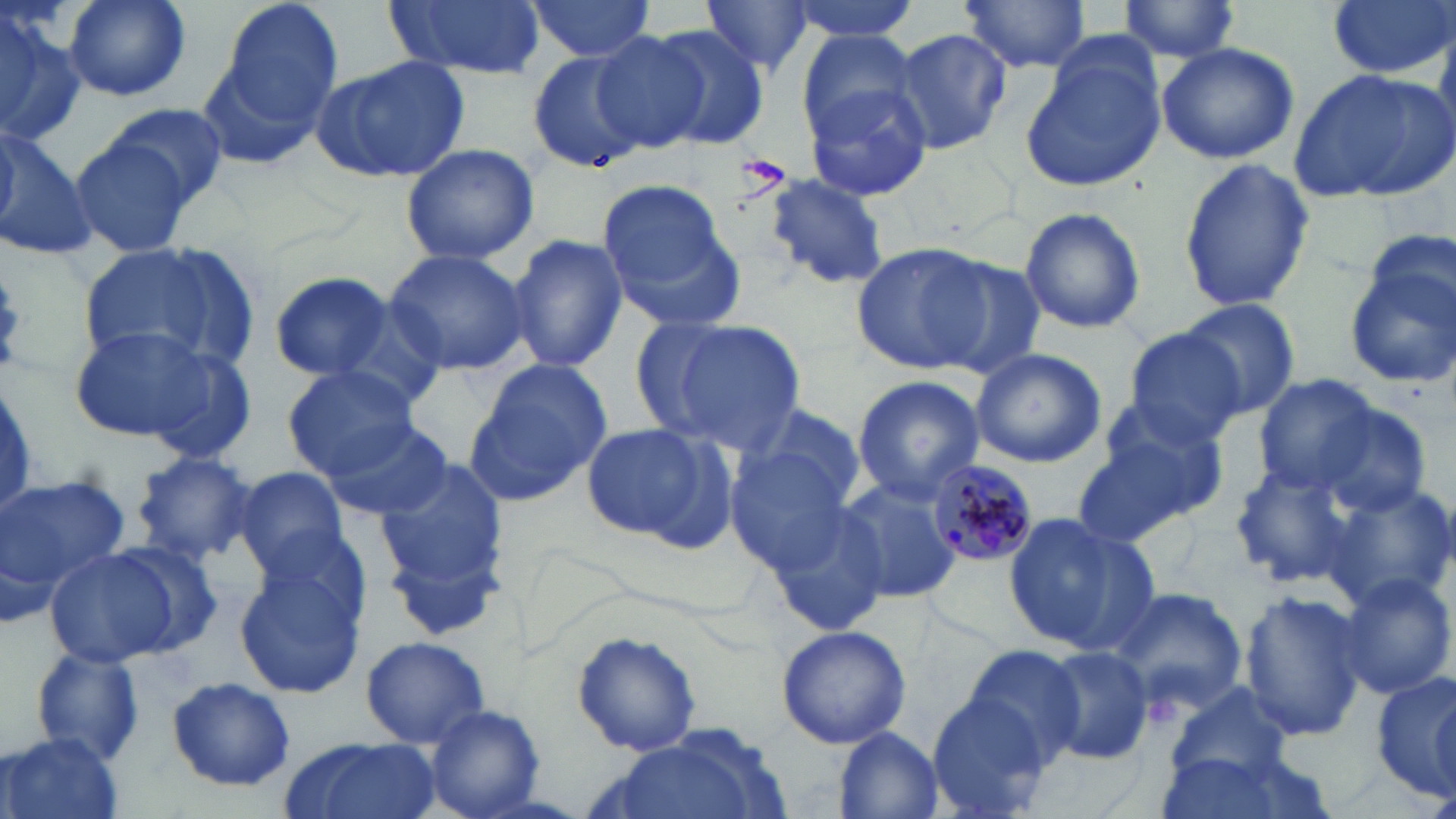
Summary:
  - Coordinate format: approximate bounding boxes as (x1, y1, x2, y2) in pixels
  - Uninfected red blood cell locations: (64, 0, 191, 102), (383, 0, 549, 80), (699, 0, 814, 80), (787, 0, 920, 46), (958, 0, 1094, 72), (1325, 0, 1452, 80), (521, 1, 660, 61), (224, 2, 344, 126), (1113, 2, 1245, 63), (0, 5, 86, 148), (644, 24, 770, 151), (888, 27, 1012, 155), (590, 30, 713, 150), (797, 30, 931, 151), (1023, 32, 1170, 191), (1155, 42, 1300, 165), (526, 47, 652, 177), (311, 55, 472, 184), (1287, 67, 1455, 205), (804, 79, 937, 200), (109, 105, 228, 207), (0, 129, 98, 263), (69, 133, 199, 262), (400, 140, 540, 266), (1176, 156, 1315, 315), (765, 172, 890, 287), (597, 180, 742, 326), (1019, 206, 1147, 335), (508, 232, 628, 373), (850, 241, 996, 376), (78, 244, 246, 376), (384, 248, 528, 376), (1342, 248, 1456, 390), (928, 254, 1050, 381), (269, 270, 397, 385), (0, 271, 26, 372), (1177, 297, 1303, 419), (625, 319, 743, 439), (653, 319, 808, 456), (70, 325, 243, 448), (1119, 328, 1248, 446), (970, 348, 1106, 467), (465, 361, 611, 504), (282, 364, 423, 478), (1255, 374, 1384, 494), (851, 377, 985, 502), (1307, 402, 1433, 518), (737, 403, 868, 512), (1075, 404, 1233, 540), (320, 418, 458, 520), (578, 421, 727, 545), (724, 448, 856, 575), (131, 450, 260, 564), (374, 456, 514, 628), (1229, 458, 1376, 588), (232, 467, 353, 582), (834, 475, 960, 604), (0, 478, 131, 593), (1324, 481, 1456, 606), (762, 495, 894, 638), (1004, 512, 1157, 657), (43, 545, 189, 667), (233, 556, 366, 699), (1334, 572, 1454, 698), (1106, 585, 1249, 718), (1239, 589, 1365, 742), (775, 625, 912, 750), (571, 630, 704, 758), (360, 634, 490, 748), (959, 643, 1088, 765), (28, 644, 148, 769), (1039, 644, 1155, 764), (1372, 671, 1456, 800), (165, 677, 296, 791), (1167, 681, 1295, 781), (928, 694, 1055, 818), (425, 704, 547, 819), (831, 725, 944, 819), (3, 731, 124, 819), (592, 731, 775, 819), (278, 736, 442, 819), (1152, 748, 1294, 818)
  - Plasmodium malariae-infected red blood cell locations: (924, 458, 1036, 566)
  - Slide-level diagnosis: Plasmodium malariae
  - Field of view: one of a larger specimen
  - Image size: 1456×819 pixels
  - Magnification: 1000x
  - Modality: light microscopy
  - Stain: May-Grünwald-Giemsa
  - Preparation: thin blood film